Outline each blood parasite and name the species.
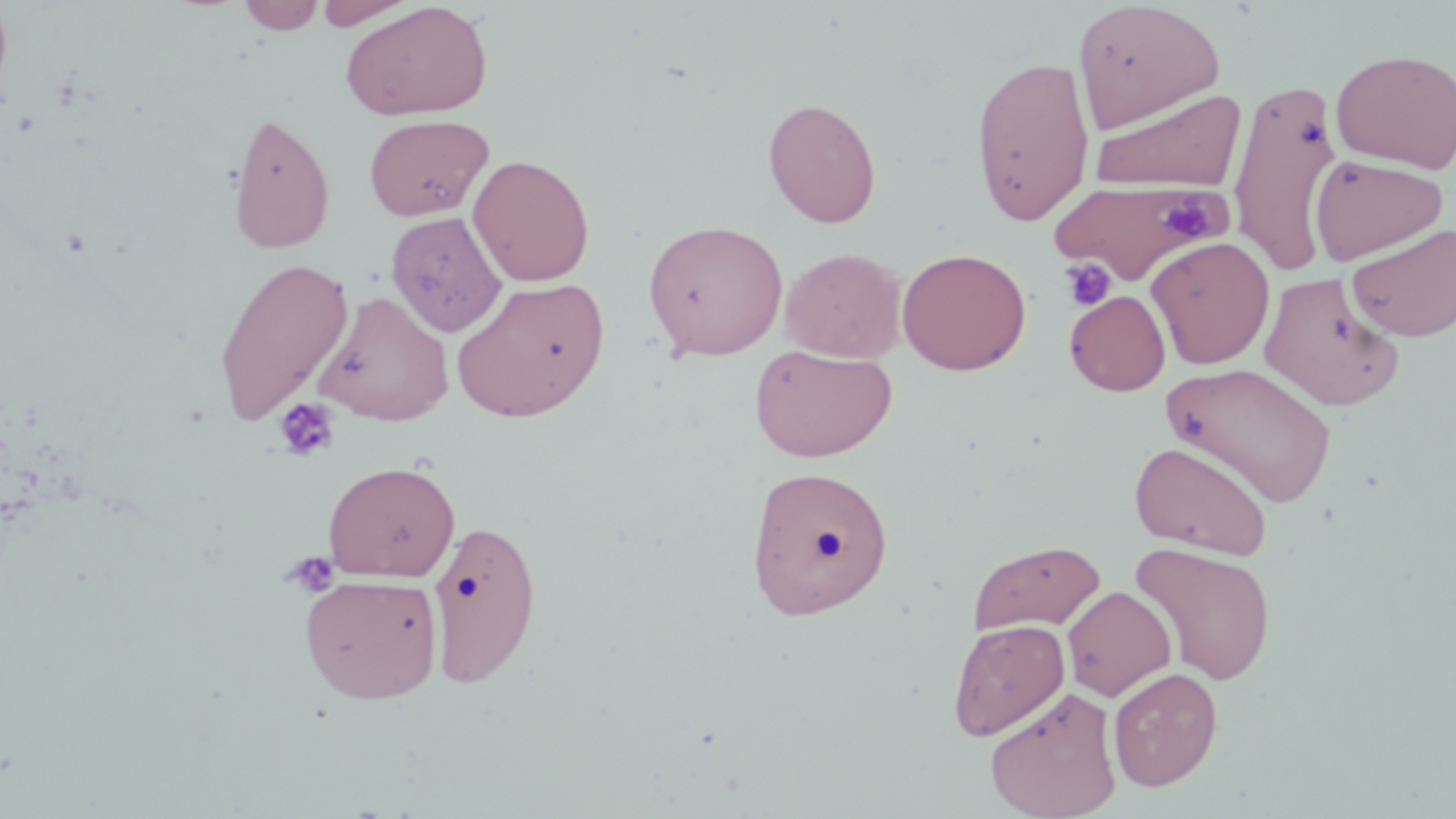

No blood parasites seen.

Approximate bounding boxes as (x1, y1, x2, y2) in pixels. Platelet locations: (1158, 195, 1217, 240), (1059, 257, 1116, 312), (273, 397, 340, 462), (280, 550, 340, 597). Uninfected red blood cell locations: (313, 0, 417, 29), (237, 1, 325, 34), (340, 1, 494, 121), (1072, 1, 1225, 133), (1331, 48, 1456, 173), (969, 54, 1095, 226), (1228, 75, 1344, 273), (1090, 88, 1246, 191), (763, 97, 882, 228), (226, 110, 336, 254), (363, 114, 494, 220), (467, 154, 595, 286), (1310, 154, 1449, 266), (1047, 177, 1228, 284), (386, 211, 507, 337), (643, 219, 788, 360), (1347, 221, 1456, 342), (1146, 235, 1275, 368), (780, 247, 906, 362), (896, 247, 1032, 375), (212, 256, 354, 429), (1259, 270, 1405, 411), (451, 277, 610, 422), (315, 290, 454, 427), (1064, 290, 1170, 396), (748, 344, 897, 462), (1162, 362, 1337, 508), (1129, 440, 1273, 560), (322, 460, 461, 582), (746, 464, 894, 620), (427, 516, 543, 689), (967, 538, 1107, 635), (1129, 542, 1277, 685), (299, 573, 443, 704), (1062, 585, 1176, 701), (947, 619, 1070, 741), (1108, 666, 1223, 791), (986, 685, 1122, 819). Slide-level diagnosis: negative for blood parasites. Captured at 1000x magnification. Image is 1456×819 pixels. One field of a larger specimen. Thin blood film. May-Grünwald-Giemsa-stained preparation. Light microscopy.